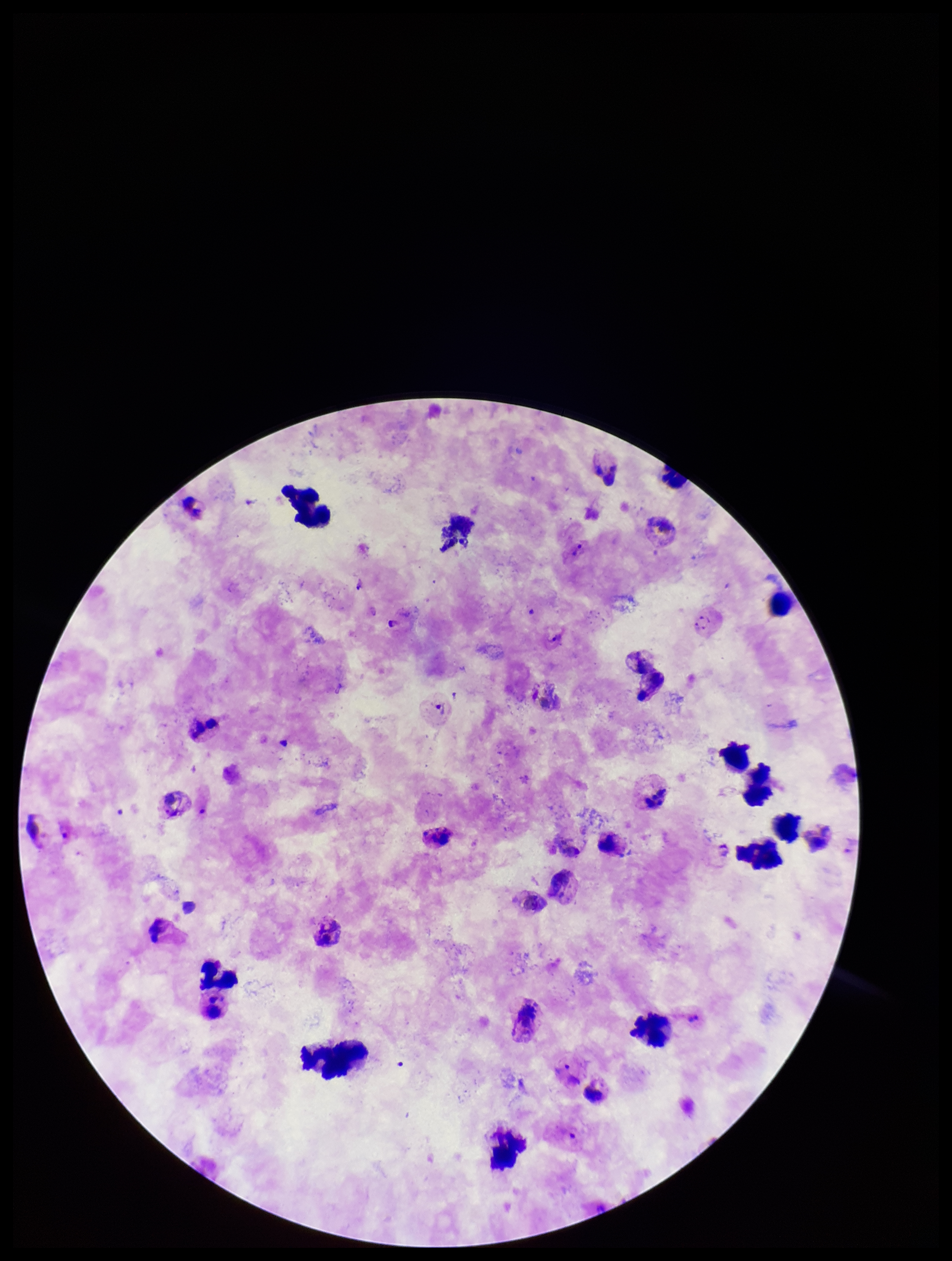

Summary:
  - Preparation: thick
  - Species reported for this patient: Plasmodium vivax
  - Capture: smartphone photograph through the microscope eyepiece
  - Parasite count: 3
  - Plasmodium parasites: identified
  - Stain: Giemsa
  - Patient malaria status: infected
  - Leukocyte count: 24
  - Image size: 952×1261 pixels
  - Field of view: one from this slide